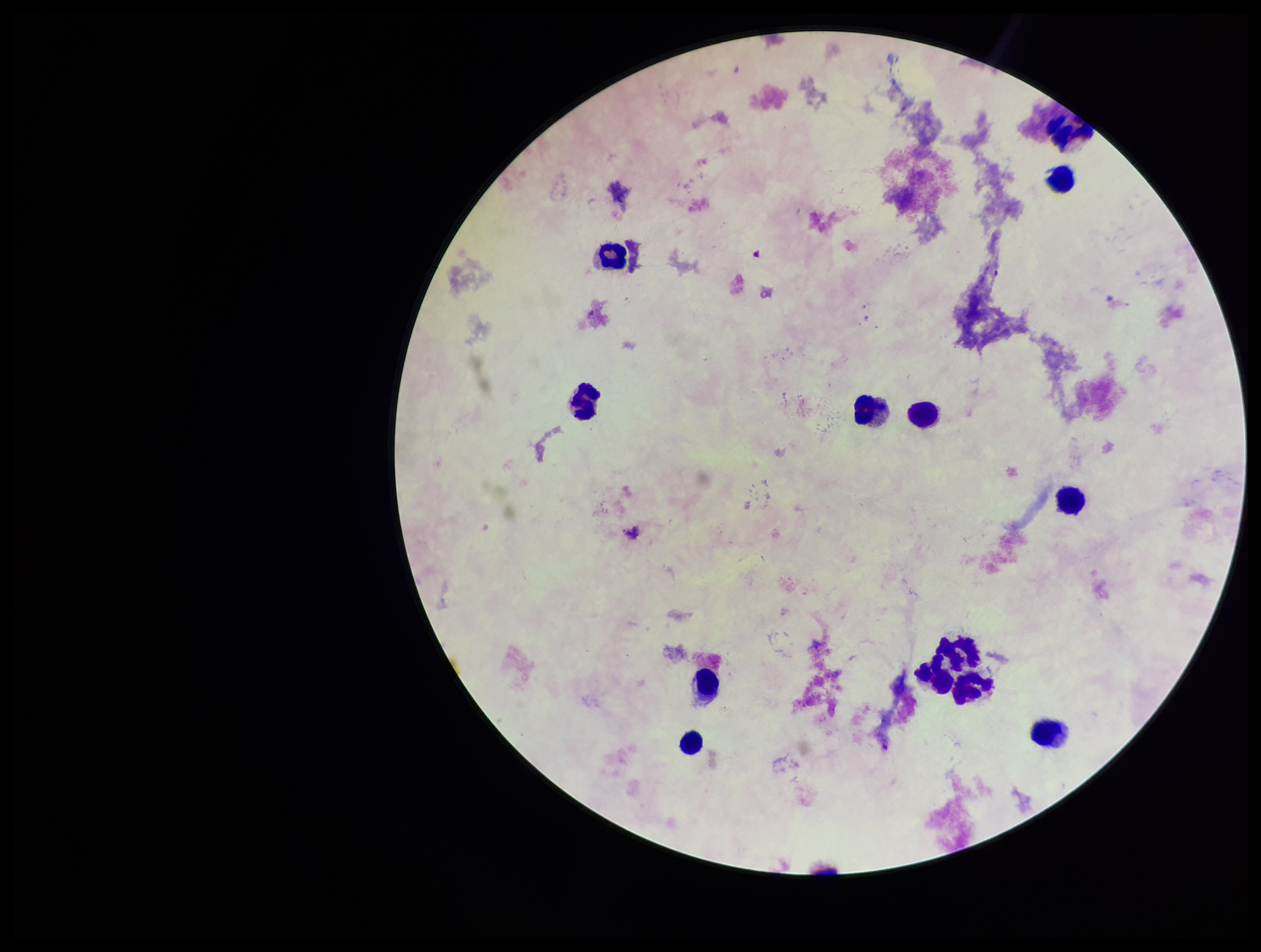
Summary:
  - Capture: smartphone photograph through the microscope eyepiece
  - Species reported for this patient: Plasmodium falciparum
  - Field of view: one from this slide
  - Plasmodium parasites: none identified
  - Parasite count: 0
  - Stain: Giemsa
  - Preparation: thick
  - Leukocyte count: 13
  - Image size: 1261×952 pixels
  - Patient malaria status: infected